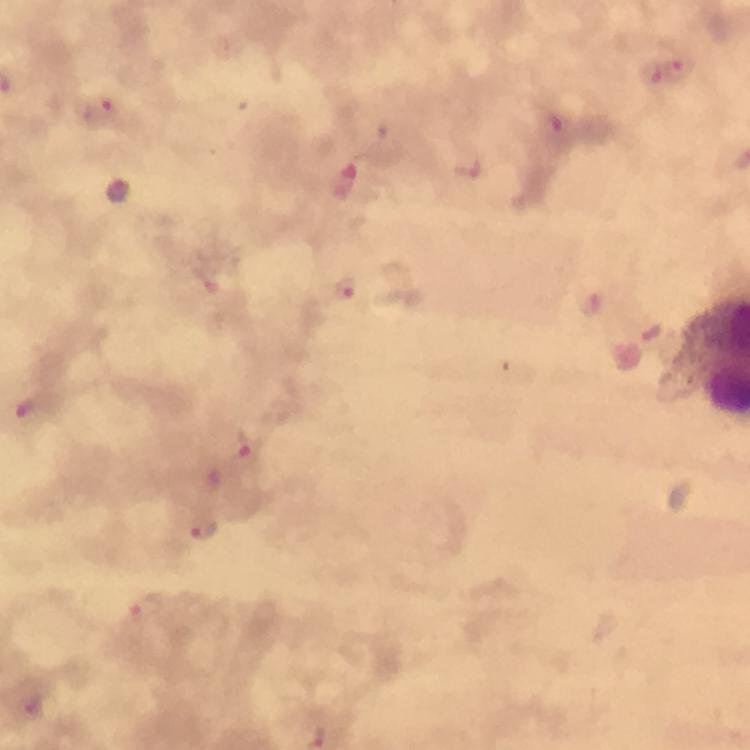

Approximate object centers, in pixels from the top-left corner. Plasmodium parasite locations: (x=681, y=68), (x=651, y=71), (x=103, y=113), (x=556, y=124), (x=467, y=168), (x=344, y=291), (x=594, y=306), (x=651, y=332), (x=31, y=407), (x=250, y=450), (x=206, y=531), (x=147, y=610). Immersion oil applied. A crop from one field of view. Thick blood smear. From a diagnostic examination for malaria. Photographed through the microscope with a smartphone camera. 100x magnification. Giemsa-stained preparation. Image is 750×750 pixels.